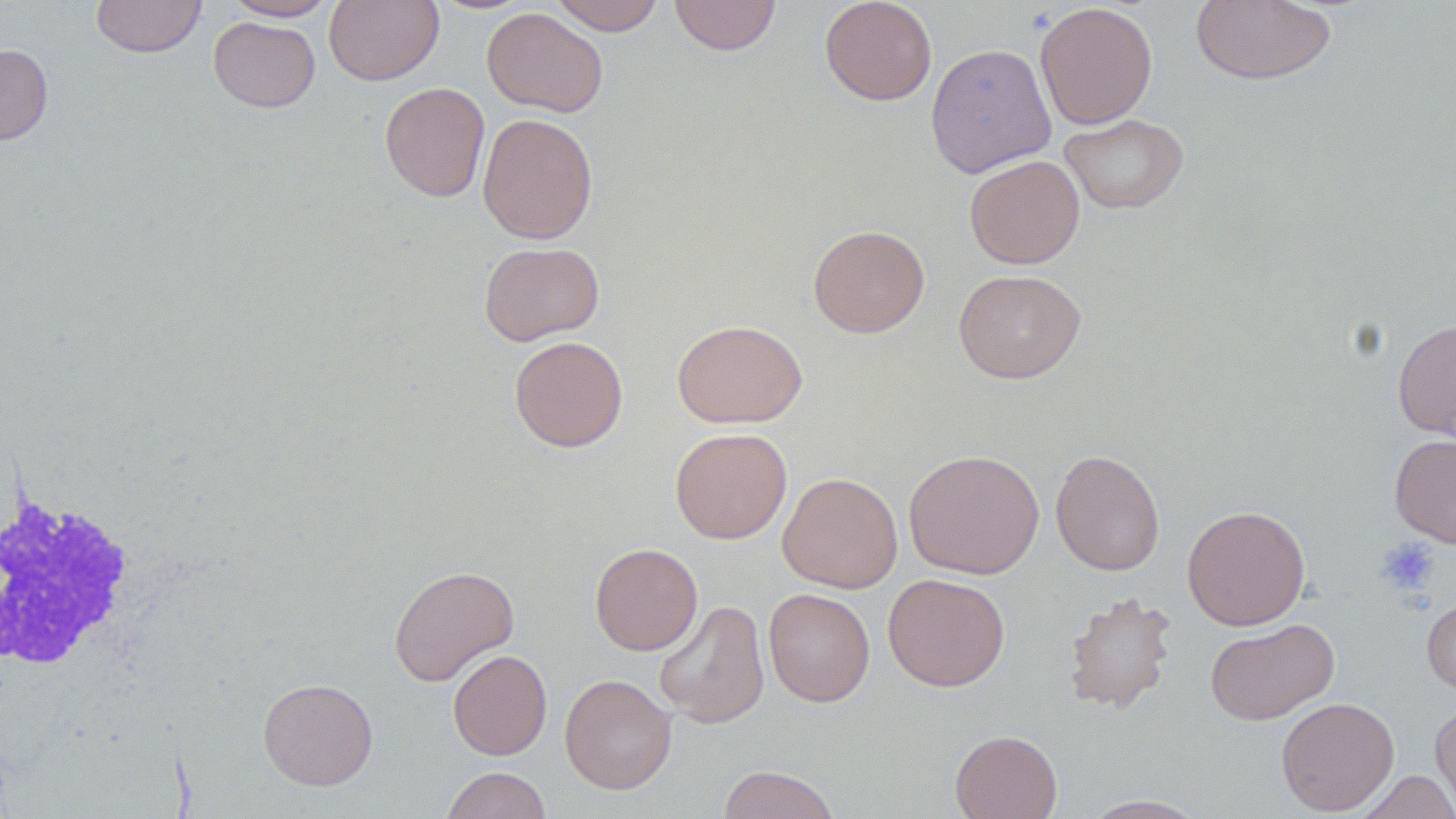 Approximate bounding boxes as (x1, y1, x2, y2) in pixels. White blood cell locations: (1, 491, 142, 678). Uninfected red blood cell locations: (91, 0, 207, 58), (224, 0, 336, 21), (324, 0, 444, 86), (549, 0, 666, 35), (669, 0, 782, 56), (819, 0, 937, 106), (1190, 1, 1337, 86), (1034, 2, 1158, 130), (482, 7, 608, 117), (208, 17, 320, 112), (925, 42, 1056, 178), (0, 43, 53, 145), (379, 82, 489, 202), (477, 112, 599, 244), (1058, 113, 1189, 215), (964, 155, 1085, 269), (807, 224, 930, 338), (479, 241, 605, 346), (954, 268, 1086, 384), (671, 319, 808, 428), (1393, 319, 1456, 441), (509, 335, 628, 452), (670, 427, 792, 544), (1390, 433, 1456, 548), (904, 448, 1044, 579), (1050, 449, 1166, 575), (777, 472, 903, 593), (1182, 504, 1311, 631), (589, 542, 703, 656), (388, 564, 519, 687), (883, 573, 1010, 691), (762, 587, 876, 707), (1063, 590, 1177, 714), (1422, 594, 1456, 698), (653, 599, 770, 729), (1205, 618, 1338, 725), (448, 649, 552, 760), (559, 673, 677, 795), (257, 678, 378, 790), (1275, 697, 1400, 815), (1429, 703, 1456, 814), (949, 729, 1063, 819), (717, 765, 842, 819), (440, 767, 552, 819), (1355, 770, 1456, 818), (1080, 795, 1210, 818). Platelet locations: (1376, 537, 1441, 596). Slide-level diagnosis: negative for blood parasites. Image is 1456×819 pixels. Thin blood film. Single field of view. May-Grünwald-Giemsa-stained preparation. 1000x magnification. Optical microscopy.